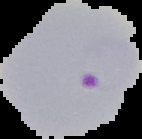
preparation = thin blood film
result = Plasmodium parasites identified
image type = segmented cell region with the area outside set to black
image size = 142×139 pixels